Name the parasite shown.
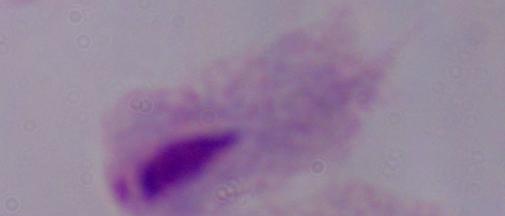
This is a trichomonad.

magnification = 1000x
modality = photomicrograph